Name the blood parasite species.
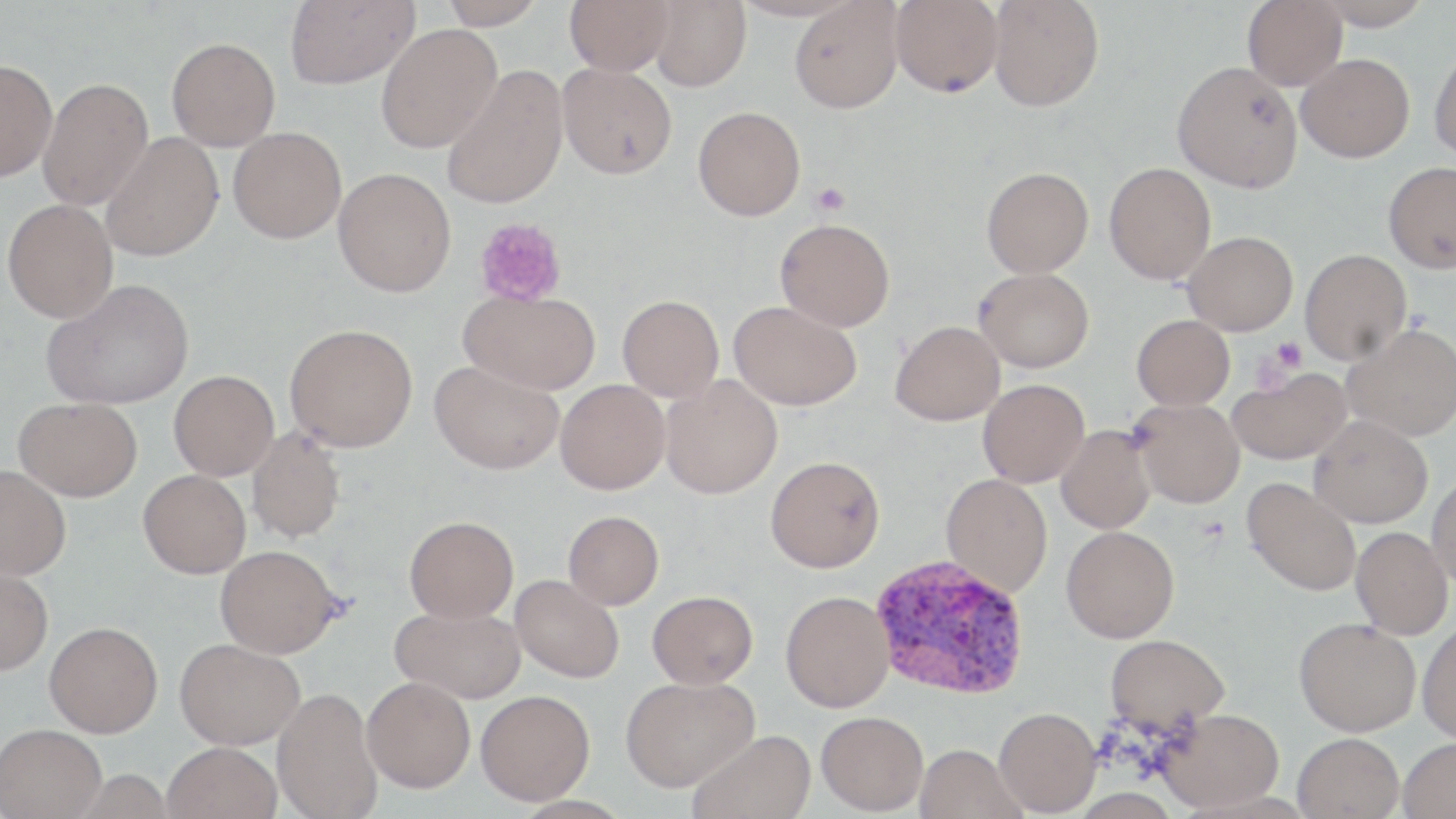
Plasmodium vivax.

magnification = 1000x
uninfected red blood cell locations = approximate bounding boxes as (x1, y1, x2, y2) in pixels: (284, 0, 419, 89), (437, 0, 547, 29), (565, 0, 674, 75), (891, 0, 1004, 97), (988, 0, 1104, 112), (1243, 0, 1347, 90), (1313, 0, 1434, 30), (649, 1, 751, 91), (790, 1, 904, 114), (375, 24, 501, 153), (166, 37, 280, 151), (1429, 46, 1456, 161), (1296, 53, 1414, 163), (0, 59, 58, 181), (1172, 61, 1303, 192), (558, 63, 677, 179), (441, 66, 570, 208), (38, 77, 153, 210), (693, 106, 806, 221), (228, 126, 347, 243), (101, 132, 223, 262), (1383, 161, 1456, 273), (1104, 163, 1216, 285), (981, 166, 1093, 278), (333, 168, 456, 297), (2, 199, 118, 323), (775, 218, 895, 331), (1183, 231, 1298, 335), (1300, 249, 1411, 365), (973, 267, 1094, 373), (42, 278, 194, 410), (460, 290, 601, 395), (617, 295, 724, 402), (729, 301, 861, 410), (1132, 315, 1234, 410), (891, 321, 1005, 426), (285, 323, 418, 452), (1342, 324, 1456, 441), (429, 359, 565, 474), (1227, 366, 1352, 465), (169, 370, 279, 480), (660, 374, 783, 499), (978, 379, 1089, 487), (556, 380, 670, 494), (13, 397, 144, 501), (1132, 399, 1245, 508), (1309, 415, 1432, 528), (1056, 425, 1156, 534), (246, 428, 346, 544), (765, 456, 885, 572), (0, 465, 71, 581), (138, 470, 251, 578), (1426, 472, 1456, 590), (940, 473, 1052, 597), (1242, 478, 1361, 596), (562, 510, 664, 609), (404, 516, 519, 622), (1061, 525, 1179, 643), (1351, 526, 1453, 639), (215, 545, 339, 658), (0, 566, 53, 675), (510, 575, 624, 683), (647, 590, 758, 688), (780, 591, 894, 713), (391, 604, 525, 703), (1294, 617, 1421, 736), (44, 621, 163, 737), (1416, 621, 1456, 743), (1105, 634, 1229, 734), (175, 638, 305, 749), (362, 676, 475, 793), (620, 676, 758, 791), (273, 688, 382, 818), (475, 690, 595, 805), (994, 707, 1102, 816), (1154, 707, 1284, 812), (816, 711, 929, 815), (0, 723, 107, 818), (688, 729, 816, 819), (1292, 732, 1404, 819), (1398, 737, 1456, 819), (162, 742, 281, 819), (915, 744, 1025, 819)
preparation = thin blood film
image size = 1456×819 pixels
Plasmodium vivax-infected red blood cell locations = approximate bounding boxes as (x1, y1, x2, y2) in pixels: (869, 553, 1029, 700)
field of view = single
modality = light microscopy
stain = May-Grünwald-Giemsa
platelet locations = approximate bounding boxes as (x1, y1, x2, y2) in pixels: (811, 182, 850, 216), (474, 217, 567, 307), (1269, 336, 1307, 373), (1248, 352, 1292, 395)